Locate every Babesia divergens-infected red blood cell.
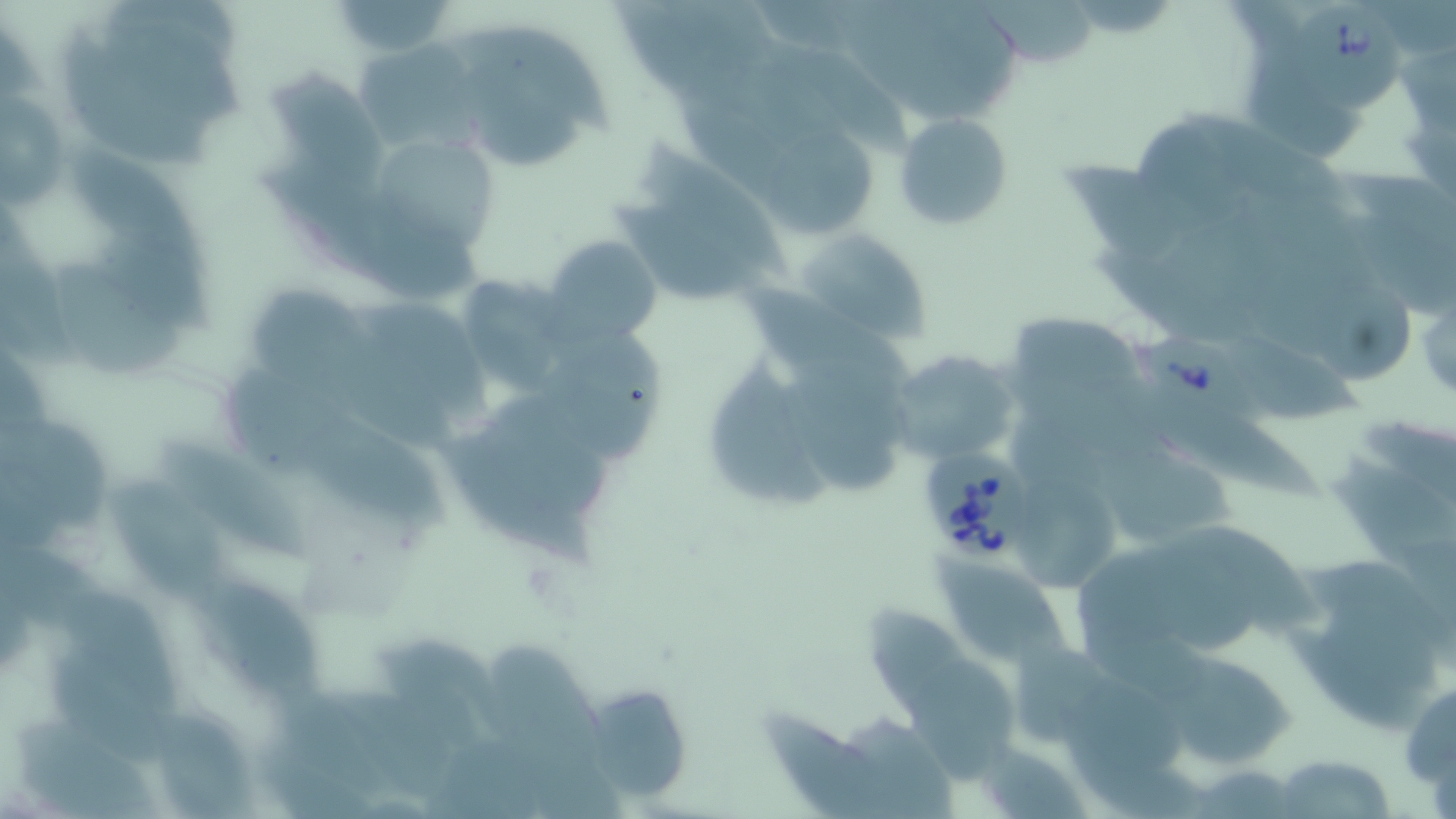
Approximate bounding boxes as (x1, y1, x2, y2) in pixels.
Babesia divergens-infected red blood cells: (1288, 3, 1409, 115), (1131, 322, 1270, 433), (916, 449, 1035, 569).

Uninfected red blood cell locations: (325, 1, 457, 57), (67, 30, 213, 172), (270, 69, 387, 183), (464, 70, 589, 176), (0, 97, 70, 213), (897, 112, 1015, 232), (761, 131, 882, 234), (633, 139, 790, 277), (62, 141, 206, 273), (386, 145, 500, 248), (795, 230, 929, 345), (543, 235, 663, 348), (56, 262, 188, 375), (467, 280, 563, 394), (1317, 284, 1421, 387), (885, 349, 1022, 468), (708, 359, 834, 514), (303, 411, 450, 529), (0, 419, 113, 533), (442, 436, 598, 569), (161, 440, 318, 565), (1329, 456, 1456, 564), (105, 478, 221, 595), (1019, 485, 1122, 594), (1178, 524, 1323, 636), (932, 549, 1073, 674), (197, 578, 326, 705), (63, 586, 185, 721), (862, 604, 975, 717), (488, 640, 608, 764), (1161, 653, 1297, 768), (908, 657, 1021, 793), (1400, 673, 1456, 801), (583, 683, 693, 805), (154, 707, 261, 819), (760, 708, 911, 819), (1272, 754, 1396, 819). Slide-level diagnosis: Babesia divergens. Optical microscopy. Captured at 1000x magnification. Thin blood smear. Image is 1456×819 pixels. May-Grünwald-Giemsa stain. One field of a larger specimen.